Give the extent of all Plasmodium falciparum-infected red blood cells.
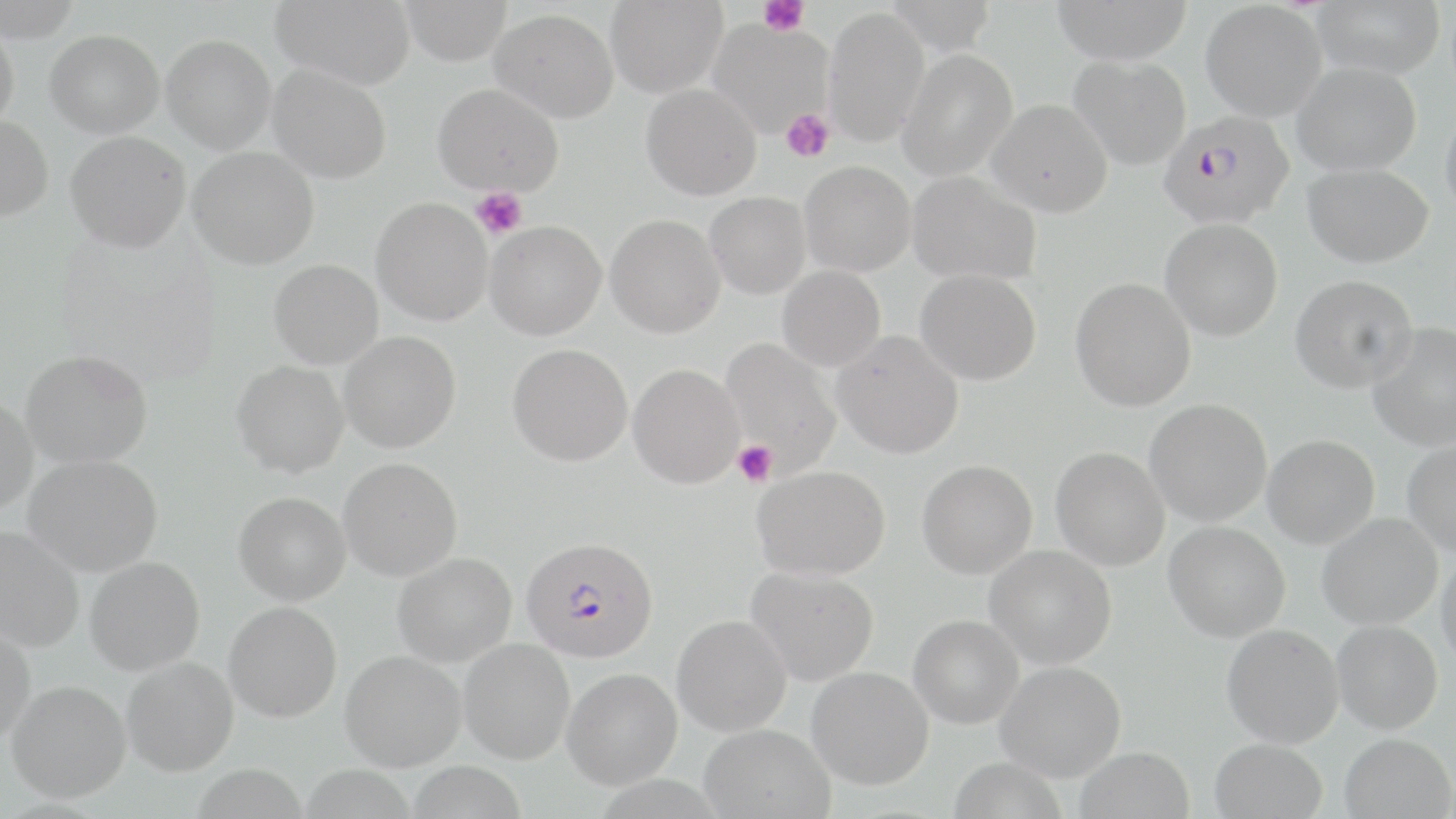

Approximate bounding boxes as (x1,y1)-(x2,y2) corner pairs in pixels.
Plasmodium falciparum-infected red blood cells: (1158,110)-(1294,227), (521,536)-(659,663).

Summary:
  - Uninfected red blood cell locations: (0,0)-(84,42), (271,0)-(416,89), (398,0)-(513,66), (605,0)-(728,98), (885,0)-(997,56), (1050,0)-(1194,64), (1311,0)-(1446,79), (1200,2)-(1327,121), (823,7)-(930,147), (490,9)-(618,123), (706,20)-(834,138), (0,23)-(19,132), (45,30)-(164,137), (161,34)-(277,154), (897,49)-(1018,180), (1068,55)-(1191,170), (1292,61)-(1423,176), (267,64)-(392,184), (433,83)-(564,196), (641,83)-(762,201), (987,99)-(1113,217), (1440,101)-(1456,221), (0,116)-(53,221), (66,131)-(190,252), (188,146)-(319,269), (800,161)-(916,276), (1303,163)-(1434,268), (907,171)-(1041,286), (705,192)-(811,299), (371,197)-(493,326), (606,214)-(725,338), (1160,218)-(1283,341), (484,220)-(607,340), (268,259)-(384,369), (778,265)-(886,371), (916,269)-(1041,386), (1290,274)-(1418,393), (1070,278)-(1196,412), (1367,324)-(1456,451), (832,330)-(964,459), (339,331)-(461,453), (720,338)-(843,476), (508,343)-(633,466), (20,350)-(153,468), (232,360)-(350,477), (628,363)-(745,489), (0,396)-(39,514), (1144,398)-(1272,526), (1262,435)-(1380,549), (1402,437)-(1456,556), (1051,446)-(1170,570), (24,455)-(163,576), (338,457)-(463,581), (916,460)-(1038,579), (753,465)-(891,580), (233,491)-(351,605), (1317,512)-(1442,630), (1163,521)-(1290,642), (0,527)-(84,653), (985,544)-(1117,669), (1436,551)-(1456,669), (392,553)-(516,668), (85,556)-(205,676), (746,565)-(880,686), (224,601)-(342,722), (908,614)-(1024,729), (672,615)-(792,736), (1331,619)-(1443,734), (0,622)-(36,745), (1222,623)-(1344,748), (459,639)-(575,764), (339,649)-(466,771), (121,657)-(239,776), (995,661)-(1126,782), (806,666)-(934,790), (562,668)-(682,789), (6,680)-(131,804), (699,724)-(835,818), (1340,733)-(1454,819), (1209,738)-(1328,819), (1074,746)-(1195,819), (947,756)-(1069,819)
  - Platelet locations: (759,0)-(809,36), (781,108)-(834,163), (471,187)-(527,239), (732,441)-(777,487)
  - Slide-level diagnosis: Plasmodium falciparum
  - Magnification: 1000x
  - Modality: light microscopy
  - Field of view: one of a larger specimen
  - Preparation: thin blood smear
  - Stain: May-Grünwald-Giemsa
  - Image size: 1456×819 pixels